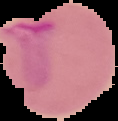 The area outside the segmented cell region is set to black. From a thin blood film. Image is 118×121 pixels. Malaria status: parasitized.